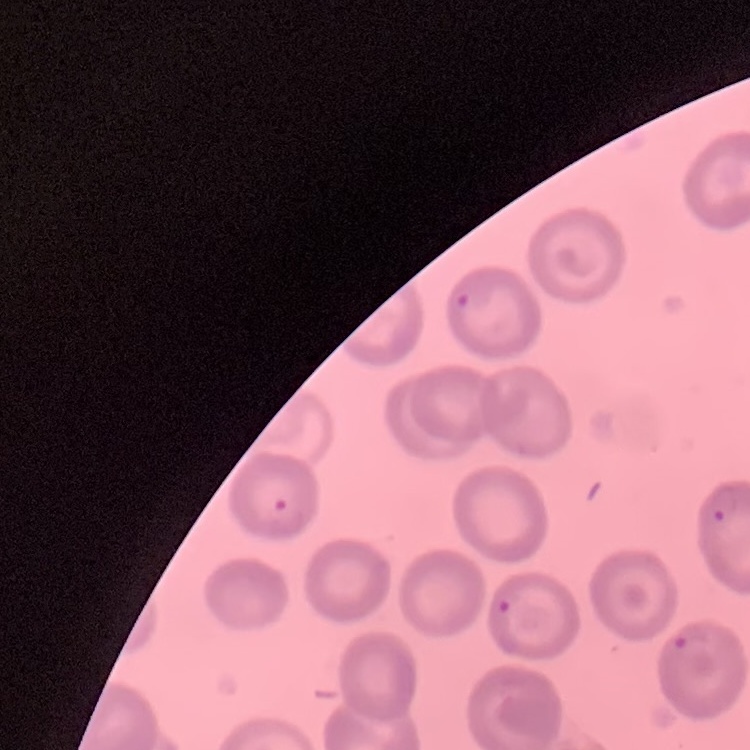

{
  "erythrocyte_morphology": "no rouleaux formation",
  "stain": "Field's or Giemsa",
  "image_type": "square crop of a larger photomicrograph",
  "preparation": "thin blood film"
}